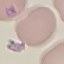
Summary:
  - Malaria status: parasitized
  - Stain: Giemsa
  - Preparation: thin blood film
  - Capture: smartphone through the microscope eyepiece
  - Image type: cell patch, automatically extracted from a larger field of view and resized to 64 × 64 pixels